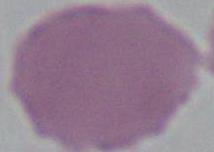
modality = micrograph
identification = red blood cell
magnification = 1000x